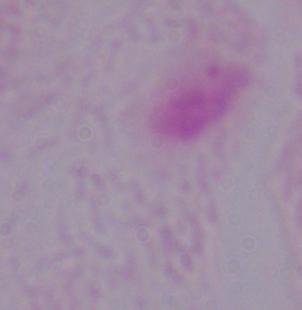
Summary:
  - Modality: micrograph
  - Magnification: 1000x
  - Identification: trichomonad